Classify this cell by malaria status.
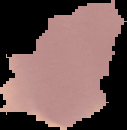
It is uninfected.

image type = segmented cell region on a black background
preparation = thin blood smear
image size = 127×130 pixels